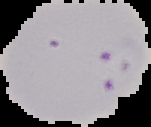
From a thin blood smear. Image is 151×127 pixels. Malaria status: parasitized. Segmented cell region on a black background.